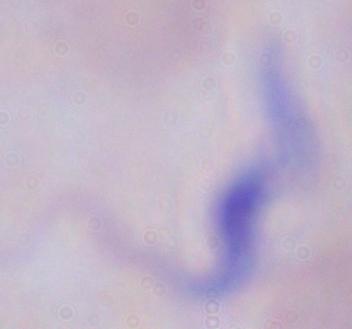

identification = trypanosome
magnification = 1000x
modality = micrograph